Assess the morphology of the red blood cells.
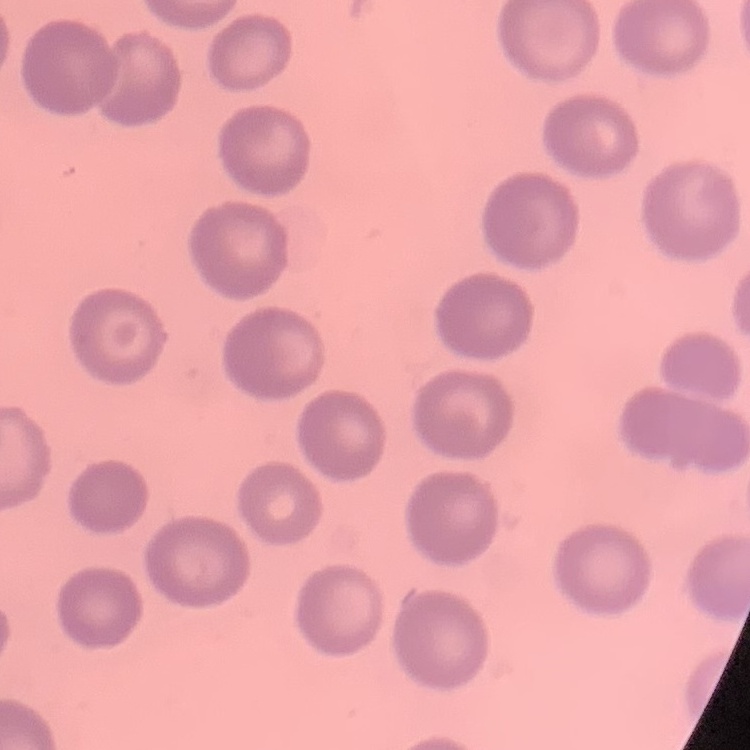

They show no rouleaux formation.

Field's or Giemsa stain. One tile cut from a larger photomicrograph. Thin blood smear.